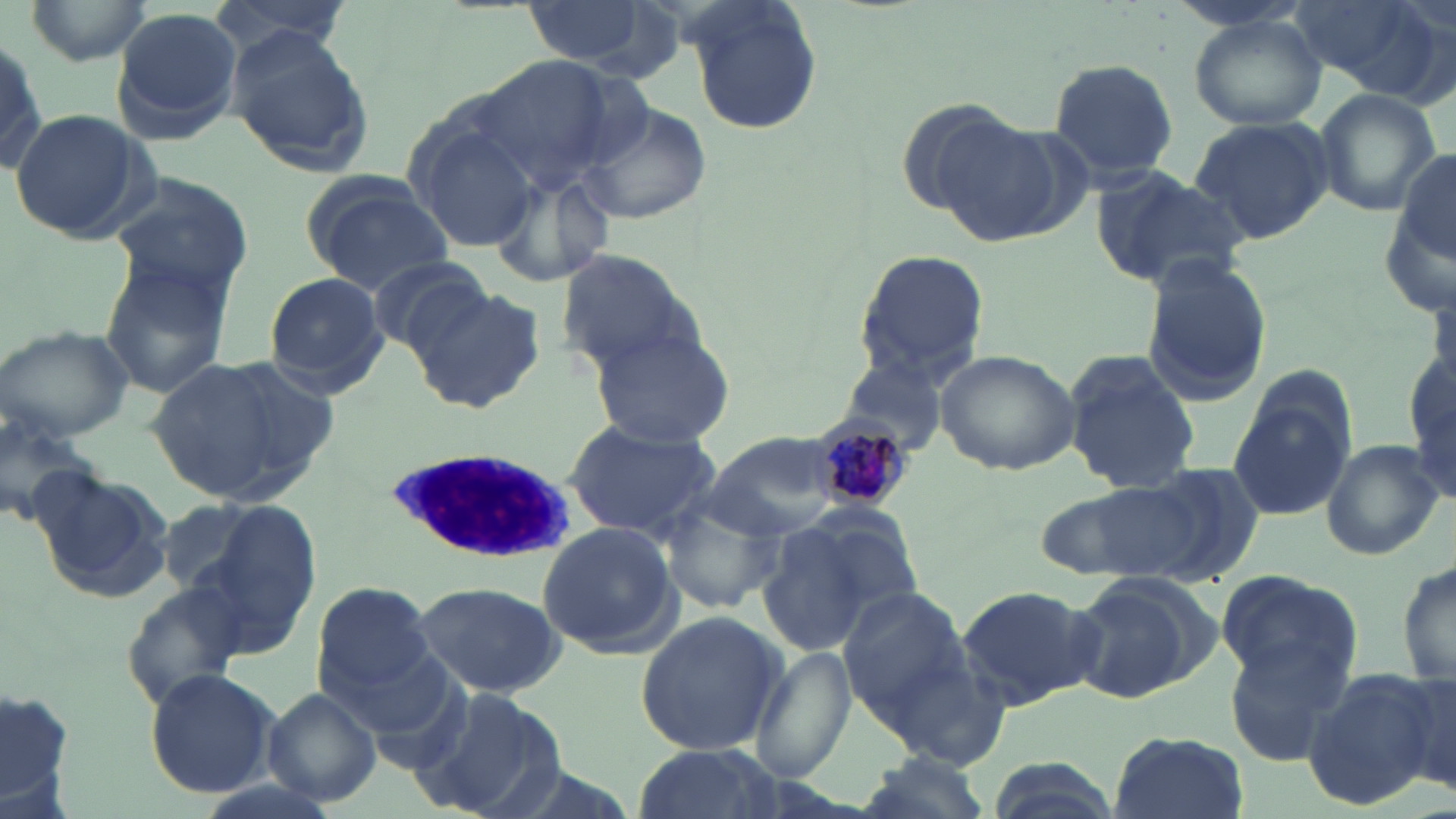
Summary:
  - Coordinate format: approximate bounding boxes as named x1/y1/x2/y2 corners in pixels
  - Uninfected red blood cell locations: (x1=23, y1=0, x2=153, y2=66), (x1=209, y1=0, x2=353, y2=63), (x1=675, y1=0, x2=825, y2=135), (x1=513, y1=1, x2=660, y2=70), (x1=1288, y1=1, x2=1440, y2=95), (x1=111, y1=9, x2=245, y2=145), (x1=1187, y1=13, x2=1328, y2=131), (x1=0, y1=30, x2=50, y2=181), (x1=226, y1=32, x2=375, y2=177), (x1=473, y1=54, x2=622, y2=192), (x1=1047, y1=57, x2=1180, y2=182), (x1=1312, y1=87, x2=1440, y2=217), (x1=576, y1=99, x2=711, y2=227), (x1=9, y1=108, x2=155, y2=245), (x1=404, y1=112, x2=547, y2=256), (x1=1188, y1=116, x2=1334, y2=246), (x1=930, y1=117, x2=1069, y2=247), (x1=1394, y1=149, x2=1454, y2=262), (x1=482, y1=158, x2=620, y2=294), (x1=1089, y1=167, x2=1250, y2=293), (x1=104, y1=173, x2=257, y2=305), (x1=301, y1=175, x2=452, y2=291), (x1=849, y1=246, x2=990, y2=389), (x1=555, y1=250, x2=699, y2=372), (x1=363, y1=255, x2=493, y2=356), (x1=1138, y1=255, x2=1274, y2=405), (x1=97, y1=258, x2=238, y2=398), (x1=262, y1=273, x2=388, y2=390), (x1=406, y1=282, x2=547, y2=415), (x1=587, y1=323, x2=737, y2=448), (x1=0, y1=326, x2=132, y2=441), (x1=1407, y1=337, x2=1455, y2=508), (x1=935, y1=349, x2=1082, y2=475), (x1=1062, y1=352, x2=1201, y2=496), (x1=145, y1=354, x2=325, y2=505), (x1=834, y1=354, x2=953, y2=458), (x1=1230, y1=394, x2=1353, y2=523), (x1=0, y1=396, x2=99, y2=531), (x1=560, y1=417, x2=725, y2=541), (x1=699, y1=431, x2=865, y2=538), (x1=1319, y1=438, x2=1443, y2=560), (x1=1136, y1=460, x2=1270, y2=585), (x1=31, y1=467, x2=173, y2=603), (x1=1037, y1=477, x2=1208, y2=585), (x1=658, y1=492, x2=787, y2=613), (x1=153, y1=498, x2=269, y2=599), (x1=183, y1=500, x2=321, y2=650), (x1=758, y1=512, x2=907, y2=657), (x1=536, y1=521, x2=681, y2=656), (x1=1396, y1=557, x2=1456, y2=690), (x1=1213, y1=569, x2=1361, y2=692), (x1=1064, y1=572, x2=1220, y2=707), (x1=122, y1=580, x2=253, y2=706), (x1=313, y1=581, x2=439, y2=701), (x1=409, y1=581, x2=565, y2=698), (x1=833, y1=583, x2=975, y2=724), (x1=955, y1=584, x2=1100, y2=710), (x1=634, y1=608, x2=788, y2=756), (x1=1221, y1=628, x2=1359, y2=766), (x1=751, y1=644, x2=856, y2=784), (x1=145, y1=668, x2=278, y2=797), (x1=1303, y1=668, x2=1449, y2=807), (x1=0, y1=684, x2=79, y2=814), (x1=421, y1=685, x2=566, y2=819), (x1=261, y1=686, x2=384, y2=808), (x1=1106, y1=729, x2=1248, y2=819), (x1=632, y1=741, x2=780, y2=819), (x1=851, y1=752, x2=992, y2=818), (x1=981, y1=756, x2=1126, y2=819)
  - Plasmodium malariae-infected red blood cell locations: (x1=817, y1=422, x2=911, y2=511)
  - White blood cell locations: (x1=386, y1=448, x2=584, y2=564)
  - Slide-level diagnosis: Plasmodium malariae
  - Stain: May-Grünwald-Giemsa
  - Image size: 1456×819 pixels
  - Preparation: thin blood film
  - Magnification: 1000x
  - Modality: light microscopy
  - Field of view: one of a larger specimen